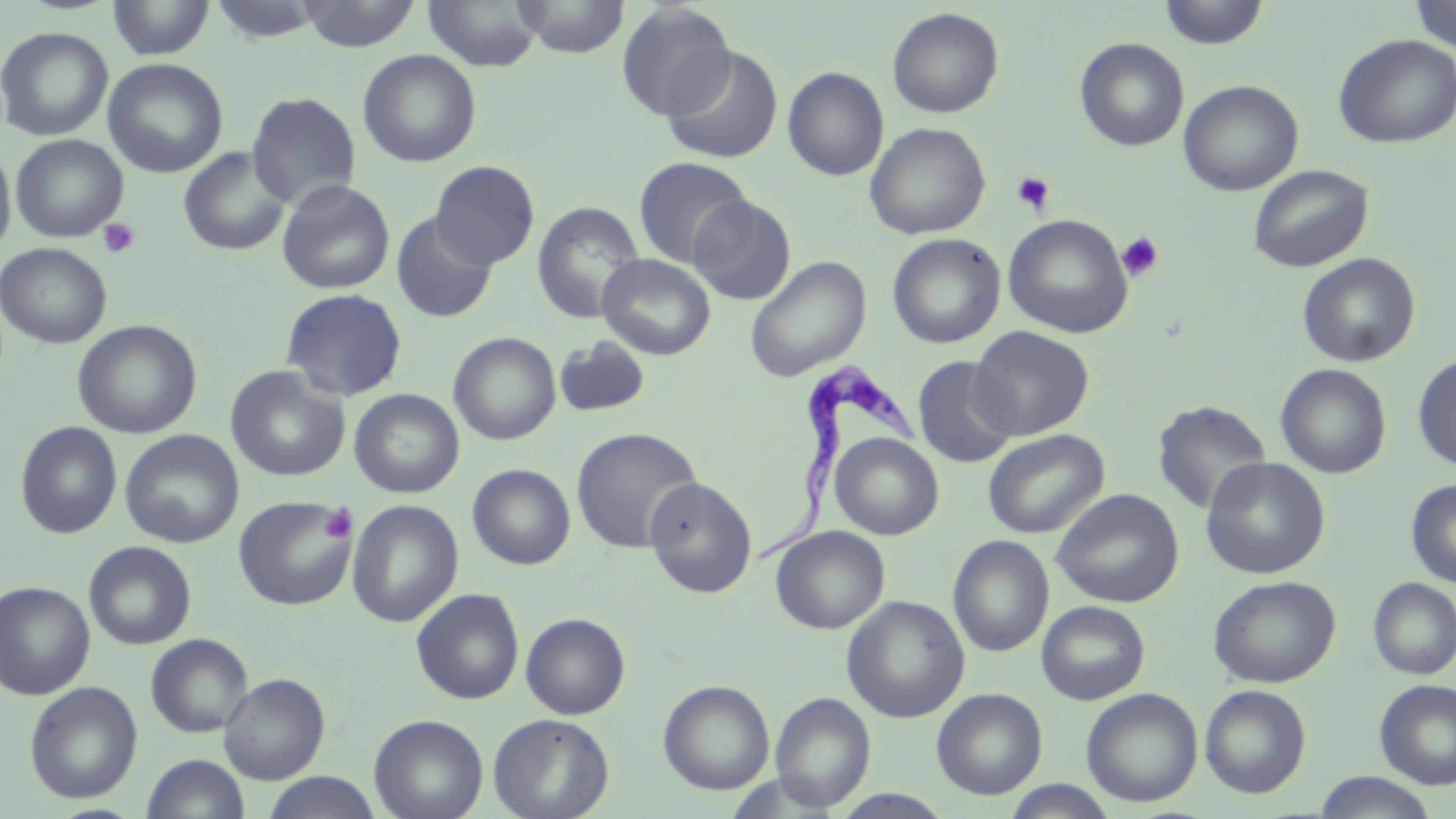
Approximate bounding boxes as (x1, y1, x2, y2) in pixels. Platelet locations: (1012, 171, 1055, 215), (98, 218, 141, 259), (1117, 232, 1164, 281), (319, 504, 357, 544). Trypanosoma brucei locations: (751, 361, 924, 572). Uninfected red blood cell locations: (107, 0, 215, 61), (294, 0, 423, 52), (422, 0, 544, 72), (513, 0, 630, 59), (1156, 0, 1270, 49), (1408, 0, 1456, 54), (208, 1, 327, 43), (616, 2, 736, 121), (886, 7, 1004, 118), (1, 26, 114, 142), (1333, 34, 1456, 149), (1074, 37, 1190, 152), (660, 46, 784, 165), (357, 49, 482, 168), (102, 58, 229, 178), (783, 66, 889, 181), (1178, 79, 1303, 197), (246, 92, 361, 210), (864, 122, 991, 240), (10, 134, 129, 243), (0, 143, 16, 260), (177, 146, 291, 256), (633, 156, 753, 269), (431, 160, 540, 269), (1248, 163, 1374, 273), (276, 179, 396, 295), (689, 195, 797, 305), (532, 201, 645, 324), (390, 211, 498, 324), (1003, 214, 1133, 339), (887, 233, 1006, 349), (0, 243, 112, 349), (597, 253, 716, 360), (1297, 253, 1420, 368), (744, 255, 872, 382), (279, 288, 408, 402), (72, 319, 202, 439), (968, 326, 1094, 441), (448, 332, 561, 445), (553, 336, 651, 419), (1413, 353, 1456, 474), (912, 356, 1018, 469), (1275, 363, 1392, 479), (225, 367, 349, 482), (349, 388, 464, 498), (1152, 399, 1272, 516), (15, 421, 122, 539), (570, 426, 703, 554), (982, 428, 1109, 539), (119, 429, 244, 549), (829, 433, 943, 540), (1201, 456, 1330, 580), (467, 463, 576, 569), (644, 477, 758, 598), (1406, 479, 1456, 588), (1051, 488, 1184, 608), (233, 495, 358, 611), (346, 499, 464, 627), (771, 526, 890, 634), (948, 535, 1054, 657), (83, 541, 196, 650), (1208, 575, 1341, 688), (1368, 577, 1456, 680), (0, 581, 95, 700), (411, 588, 525, 705), (841, 595, 970, 723), (1036, 600, 1151, 705), (520, 612, 631, 720), (145, 633, 254, 738), (218, 673, 330, 784), (1374, 679, 1456, 790), (658, 680, 775, 794), (24, 681, 143, 804), (1199, 684, 1311, 798), (931, 688, 1047, 800), (1081, 688, 1203, 807), (770, 691, 876, 810), (488, 713, 614, 819), (369, 714, 488, 819), (141, 753, 250, 819), (261, 771, 382, 819), (1312, 771, 1440, 818), (722, 772, 840, 817), (1000, 779, 1118, 818), (830, 789, 954, 819). Slide-level diagnosis: Trypanosoma brucei. Captured at 1000x magnification. May-Grünwald-Giemsa stain. Single field of view. Image is 1456×819 pixels. Optical microscopy. Thin blood film.